State which cell type is depicted.
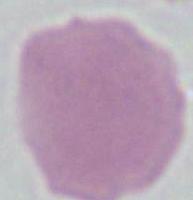

An erythrocyte.

magnification = 1000x
modality = photomicrograph